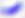

Summary:
  - Identification: Toxoplasma gondii
  - Modality: micrograph
  - Magnification: 400x